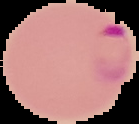
result = malaria parasites detected
preparation = thin blood film
image type = cell region segmented out of the field of view; surrounding area masked to black
image size = 139×124 pixels